Assess the morphology of the red blood cells.
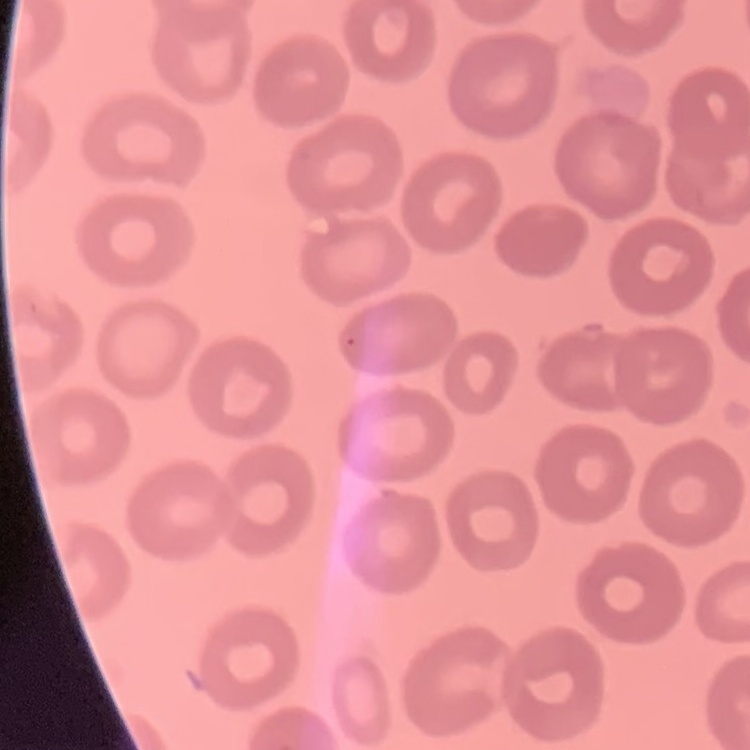

No rouleaux formation.

preparation = thin peripheral smear
image type = one tile cut from a larger photomicrograph
stain = Field's or Giemsa